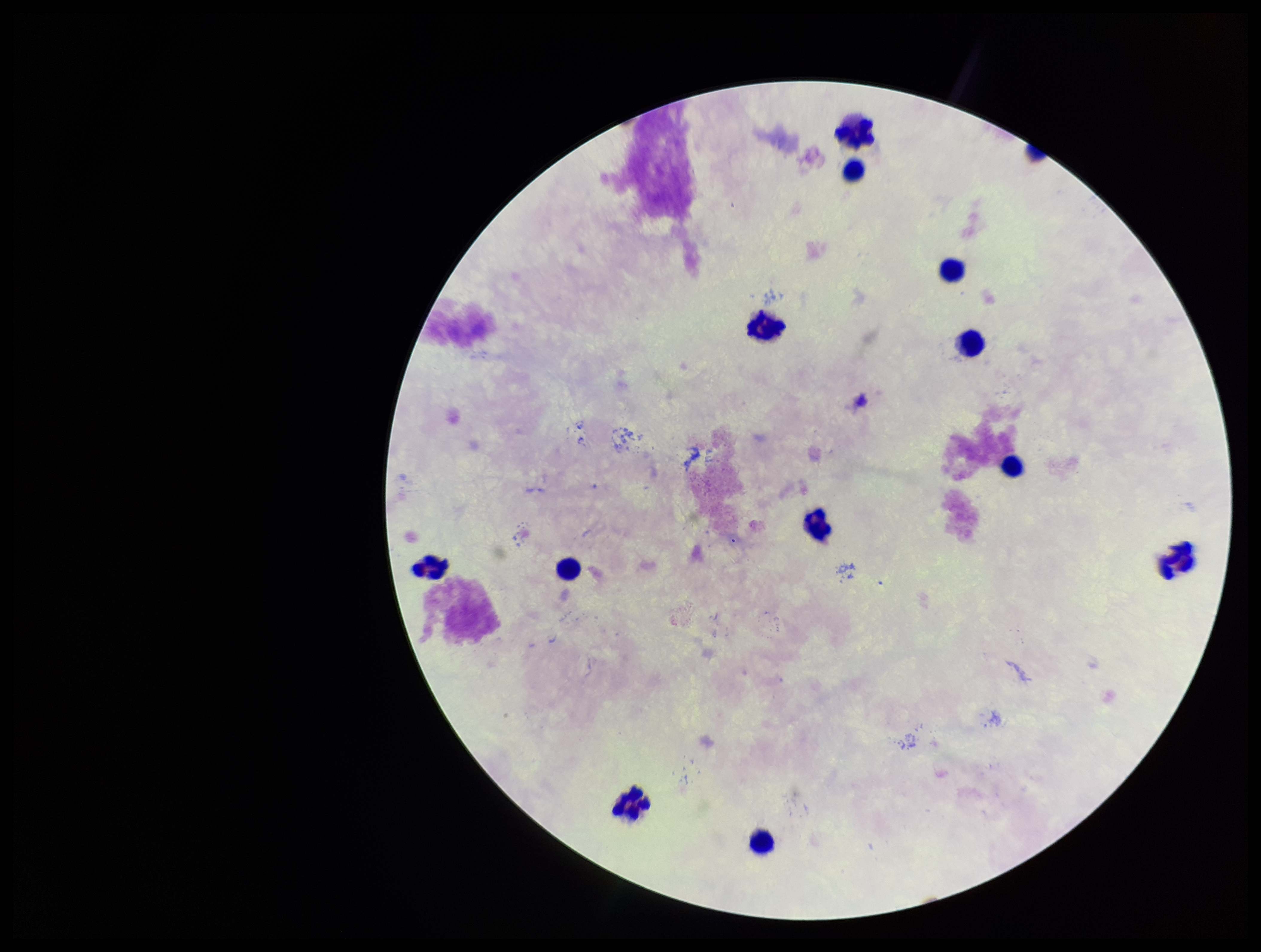
preparation = thick blood smear
leukocyte count = 12
Plasmodium parasites = none identified
capture = smartphone photograph through the microscope eyepiece
stain = Giemsa
patient malaria status = negative
field of view = single
image size = 1261×952 pixels
parasite count = 0